Assess this cell for malaria.
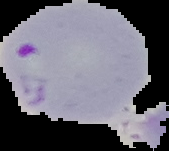

Parasitized.

Summary:
  - Image size: 169×151 pixels
  - Image type: cell region segmented out of the field of view; surrounding area masked to black
  - Preparation: thin blood film